Locate and identify every blood parasite.
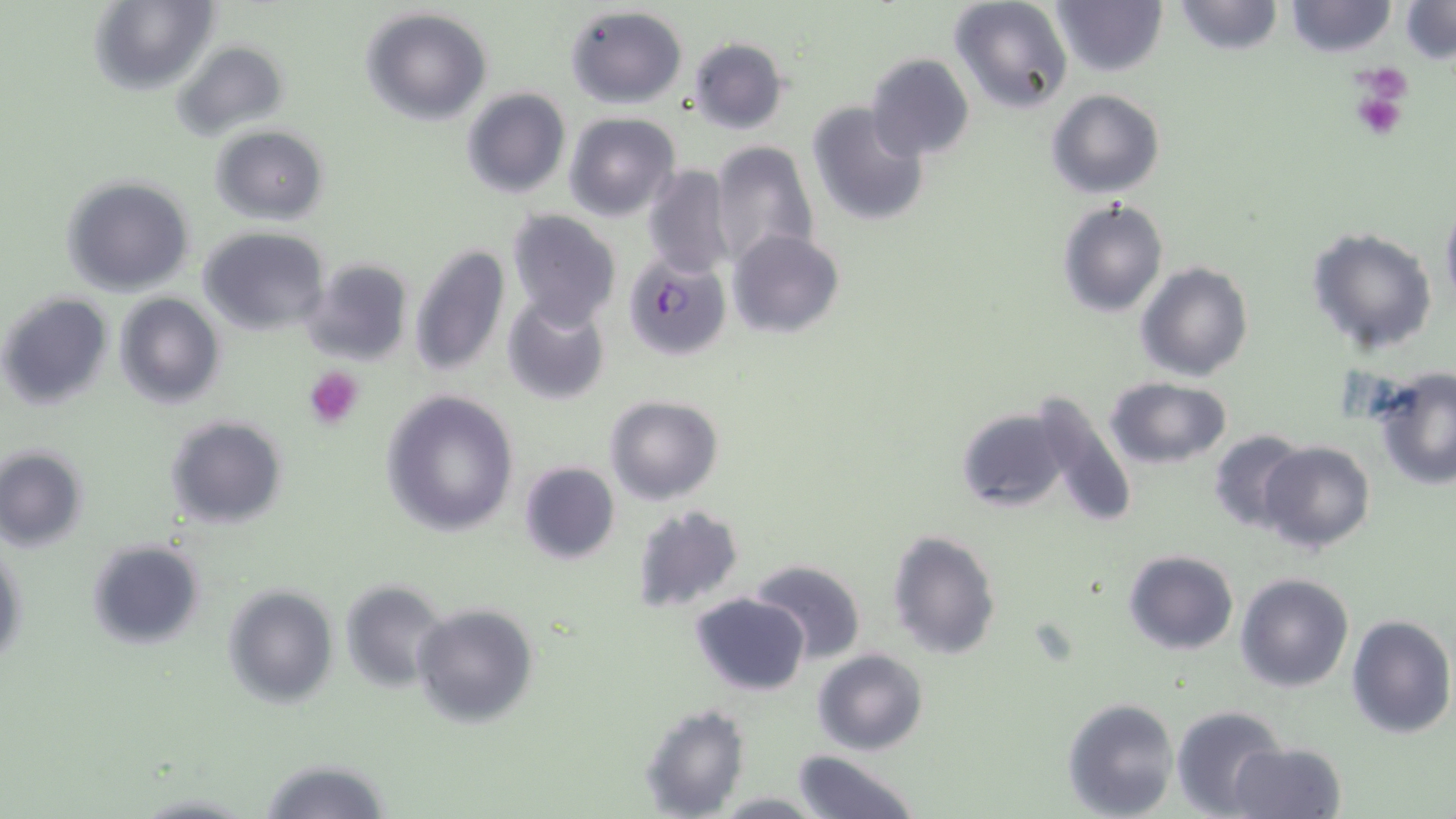

Approximate bounding boxes as [x1, y1, x2, y2] in pixels.
Plasmodium falciparum-infected red blood cells: [625, 255, 732, 361].
No Plasmodium ovale, Plasmodium malariae, Plasmodium vivax, Babesia divergens, or Trypanosoma brucei observed.

slide_level_diagnosis: Plasmodium falciparum
platelet_locations: 'approximate bounding boxes as [x1, y1, x2, y2] in pixels: [1351, 64, 1413, 117], [1351, 88, 1408, 140], [303, 366, 365, 429]'
magnification: 1000x
modality: light microscopy
preparation: thin blood smear
uninfected_red_blood_cell_locations: 'approximate bounding boxes as [x1, y1, x2, y2] in pixels: [88, 0, 218, 96], [948, 0, 1074, 113], [1049, 0, 1166, 76], [1168, 1, 1285, 54], [1284, 1, 1396, 57], [1399, 2, 1455, 66], [565, 5, 687, 108], [361, 8, 494, 125], [688, 36, 790, 134], [171, 39, 289, 141], [865, 51, 975, 162], [462, 87, 570, 198], [1047, 88, 1164, 199], [805, 102, 930, 227], [565, 113, 679, 222], [212, 124, 329, 224], [708, 141, 820, 268], [642, 164, 734, 282], [62, 176, 193, 297], [1440, 196, 1456, 308], [1056, 198, 1169, 318], [505, 211, 620, 332], [1306, 227, 1438, 357], [198, 228, 330, 334], [729, 229, 843, 337], [410, 242, 509, 380], [300, 258, 413, 366], [1137, 262, 1253, 382], [1, 291, 110, 409], [501, 292, 610, 407], [114, 293, 225, 409], [1370, 367, 1456, 491], [1104, 375, 1234, 470], [379, 390, 519, 537], [605, 396, 724, 505], [1019, 397, 1137, 526], [955, 407, 1068, 513], [165, 414, 288, 528], [1206, 429, 1309, 533], [1260, 441, 1374, 553], [0, 445, 89, 551], [518, 461, 619, 565], [630, 504, 744, 613], [886, 529, 999, 660], [1, 539, 27, 673], [87, 539, 207, 650], [1122, 550, 1238, 655], [749, 559, 867, 665], [1235, 572, 1355, 692], [340, 580, 445, 690], [223, 585, 337, 707], [691, 593, 809, 695], [413, 603, 538, 726], [1345, 614, 1455, 739], [812, 648, 928, 755], [1063, 698, 1180, 819], [640, 702, 750, 817], [1173, 706, 1288, 816], [1228, 742, 1345, 819], [792, 750, 923, 819], [256, 758, 393, 818], [713, 792, 822, 817]'
stain: May-Grünwald-Giemsa
image_size: 1456×819 pixels
field_of_view: single